Locate every Plasmodium ovale-infected red blood cell.
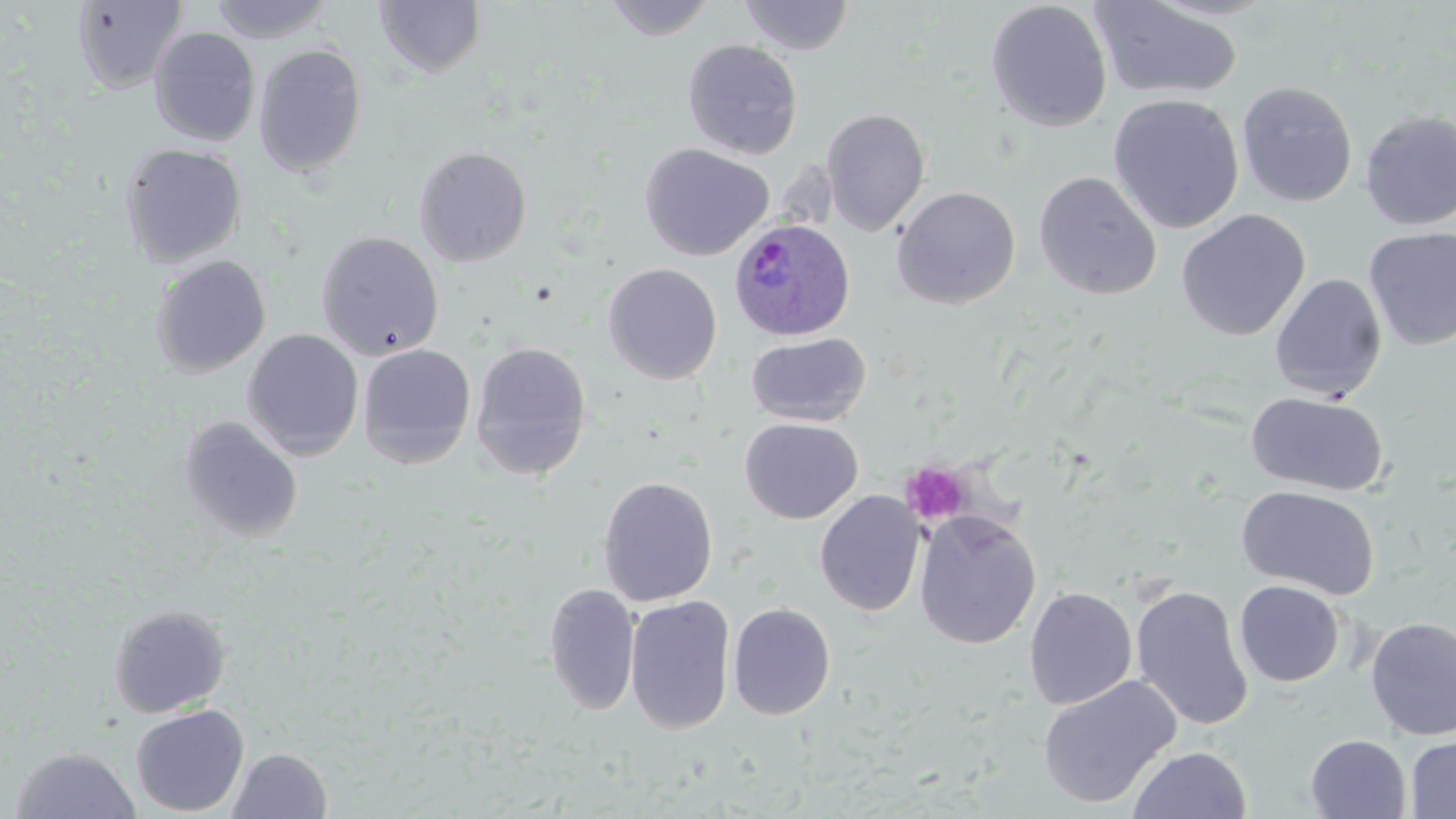
Approximate bounding boxes as [x1, y1, x2, y2] in pixels.
Plasmodium ovale-infected red blood cells: [728, 218, 854, 340].

Summary:
  - Platelet locations: [901, 461, 972, 525]
  - Uninfected red blood cell locations: [208, 0, 335, 42], [602, 0, 718, 40], [739, 0, 855, 55], [985, 0, 1113, 132], [1090, 0, 1245, 101], [71, 1, 188, 94], [374, 1, 486, 78], [149, 26, 260, 146], [151, 36, 368, 157], [683, 39, 803, 160], [254, 44, 367, 177], [1237, 81, 1358, 207], [1107, 93, 1245, 234], [821, 108, 930, 235], [1359, 110, 1456, 230], [119, 143, 247, 267], [640, 143, 774, 262], [413, 146, 532, 267], [1034, 171, 1163, 300], [892, 186, 1020, 309], [1176, 209, 1310, 341], [1363, 227, 1456, 350], [316, 231, 444, 360], [150, 255, 272, 377], [602, 263, 722, 384], [1269, 273, 1386, 401], [242, 329, 364, 460], [746, 333, 871, 426], [470, 342, 592, 481], [357, 343, 476, 469], [1246, 391, 1389, 496], [179, 417, 304, 543], [740, 417, 862, 524], [598, 476, 718, 607], [1236, 485, 1380, 599], [815, 490, 925, 616], [914, 510, 1041, 649], [1235, 580, 1344, 687], [544, 583, 640, 715], [1130, 585, 1254, 730], [1024, 587, 1137, 710], [624, 596, 736, 735], [728, 603, 836, 720], [108, 604, 232, 718], [1364, 616, 1456, 740], [1038, 675, 1181, 809], [130, 703, 249, 817], [1305, 734, 1411, 818], [1404, 734, 1456, 818], [8, 746, 142, 819], [1127, 746, 1252, 818], [227, 747, 332, 819]
  - Slide-level diagnosis: Plasmodium ovale
  - Image size: 1456×819 pixels
  - Preparation: thin blood film
  - Modality: light microscopy
  - Field of view: single
  - Stain: May-Grünwald-Giemsa
  - Magnification: 1000x